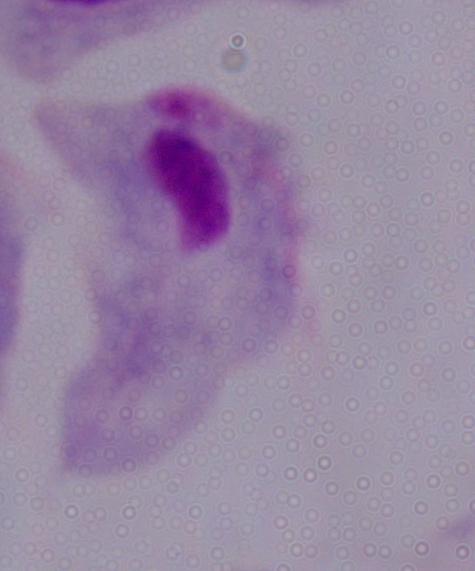 Photomicrograph. A trichomonad is shown. 1000x magnification.